Comment on the morphology of the erythrocytes.
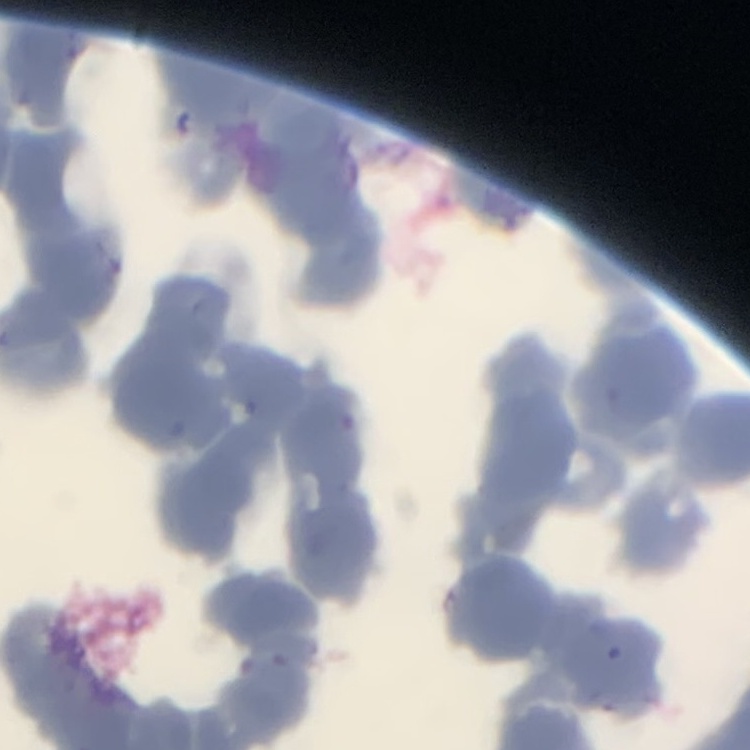
They show rouleaux formation.

stain = Field's or Giemsa
preparation = thin peripheral smear
image type = one tile cut from a larger photomicrograph